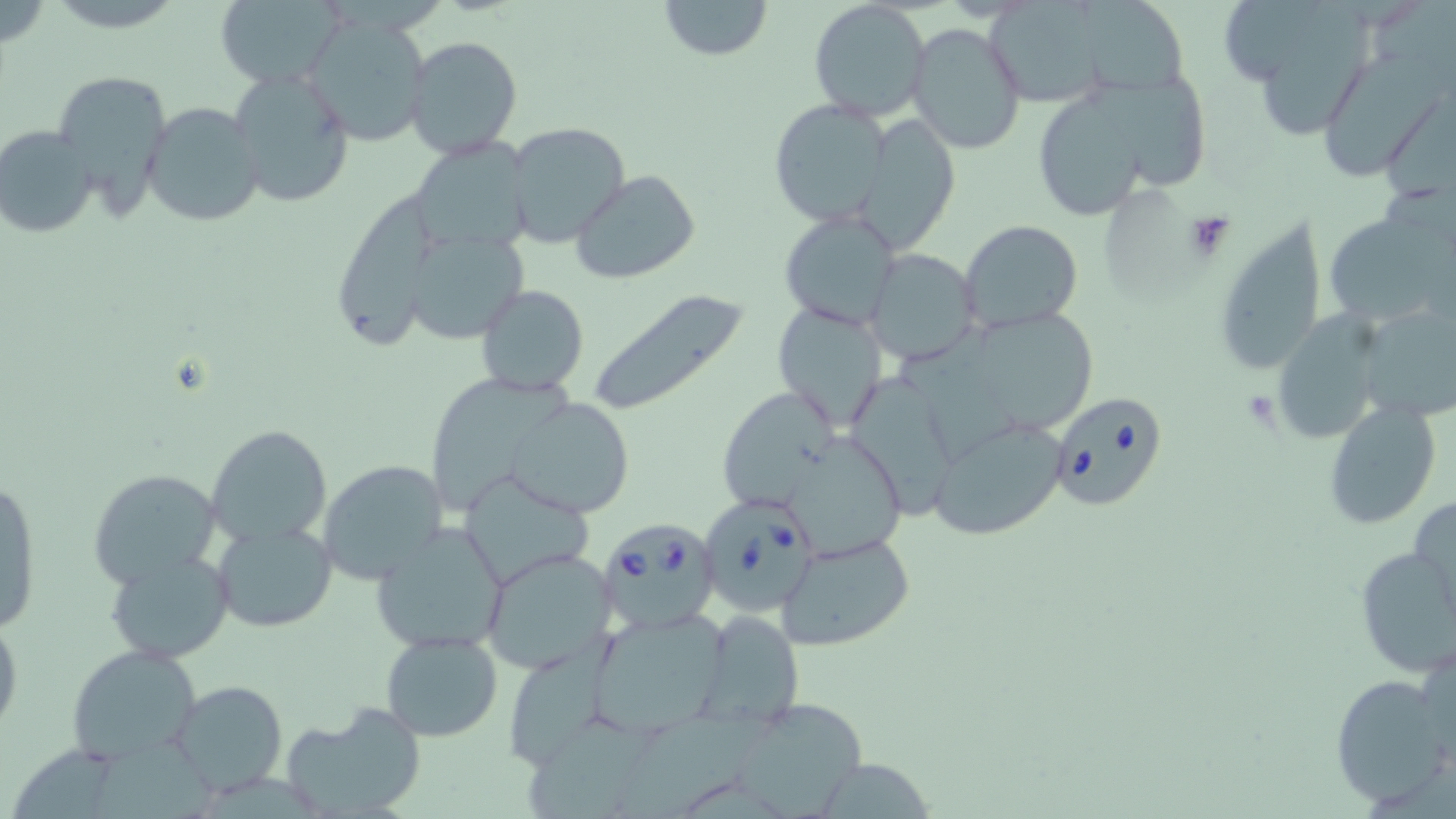

Summary:
  - Coordinate format: approximate bounding boxes as named x1/y1/x2/y2 corners in pixels
  - Platelet locations: (x1=1184, y1=210, x2=1238, y2=264)
  - Babesia divergens-infected red blood cell locations: (x1=1047, y1=389, x2=1171, y2=511), (x1=697, y1=494, x2=822, y2=617), (x1=596, y1=518, x2=719, y2=635)
  - Uninfected red blood cell locations: (x1=213, y1=0, x2=342, y2=88), (x1=659, y1=0, x2=772, y2=61), (x1=808, y1=0, x2=931, y2=120), (x1=1081, y1=0, x2=1186, y2=97), (x1=1257, y1=1, x2=1372, y2=143), (x1=304, y1=18, x2=430, y2=146), (x1=906, y1=21, x2=1028, y2=156), (x1=404, y1=35, x2=522, y2=158), (x1=1322, y1=49, x2=1444, y2=182), (x1=225, y1=66, x2=356, y2=209), (x1=52, y1=71, x2=173, y2=215), (x1=1030, y1=86, x2=1161, y2=219), (x1=769, y1=99, x2=892, y2=228), (x1=143, y1=101, x2=267, y2=228), (x1=858, y1=115, x2=961, y2=250), (x1=504, y1=121, x2=633, y2=250), (x1=0, y1=124, x2=99, y2=238), (x1=412, y1=142, x2=533, y2=257), (x1=571, y1=171, x2=701, y2=285), (x1=333, y1=197, x2=441, y2=353), (x1=1324, y1=210, x2=1451, y2=328), (x1=781, y1=211, x2=900, y2=331), (x1=1214, y1=213, x2=1329, y2=379), (x1=958, y1=219, x2=1084, y2=334), (x1=407, y1=232, x2=540, y2=349), (x1=865, y1=249, x2=980, y2=366), (x1=476, y1=284, x2=589, y2=396), (x1=587, y1=291, x2=753, y2=416), (x1=772, y1=300, x2=889, y2=432), (x1=1271, y1=308, x2=1395, y2=449), (x1=962, y1=311, x2=1101, y2=432), (x1=1364, y1=312, x2=1456, y2=431), (x1=847, y1=372, x2=962, y2=514), (x1=431, y1=377, x2=581, y2=515), (x1=721, y1=389, x2=846, y2=507), (x1=507, y1=397, x2=635, y2=519), (x1=1320, y1=401, x2=1444, y2=531), (x1=929, y1=416, x2=1069, y2=542), (x1=206, y1=424, x2=332, y2=549), (x1=782, y1=433, x2=913, y2=563), (x1=317, y1=459, x2=449, y2=583), (x1=86, y1=467, x2=224, y2=590), (x1=461, y1=472, x2=596, y2=586), (x1=1, y1=475, x2=42, y2=637), (x1=1410, y1=494, x2=1456, y2=622), (x1=372, y1=520, x2=507, y2=654), (x1=212, y1=521, x2=337, y2=632), (x1=775, y1=532, x2=916, y2=652), (x1=481, y1=547, x2=619, y2=675), (x1=1353, y1=547, x2=1455, y2=679), (x1=104, y1=549, x2=234, y2=663), (x1=692, y1=607, x2=808, y2=726), (x1=590, y1=608, x2=733, y2=732), (x1=0, y1=611, x2=23, y2=744), (x1=380, y1=630, x2=503, y2=742), (x1=67, y1=644, x2=203, y2=764), (x1=502, y1=644, x2=612, y2=770), (x1=1330, y1=674, x2=1451, y2=808), (x1=169, y1=679, x2=289, y2=796), (x1=710, y1=697, x2=876, y2=819), (x1=281, y1=703, x2=426, y2=819), (x1=618, y1=705, x2=763, y2=819), (x1=525, y1=709, x2=673, y2=819), (x1=92, y1=734, x2=243, y2=819), (x1=810, y1=757, x2=937, y2=818)
  - Slide-level diagnosis: Babesia divergens
  - Preparation: thin blood smear
  - Image size: 1456×819 pixels
  - Field of view: one of a larger specimen
  - Stain: May-Grünwald-Giemsa
  - Magnification: 1000x
  - Modality: light microscopy